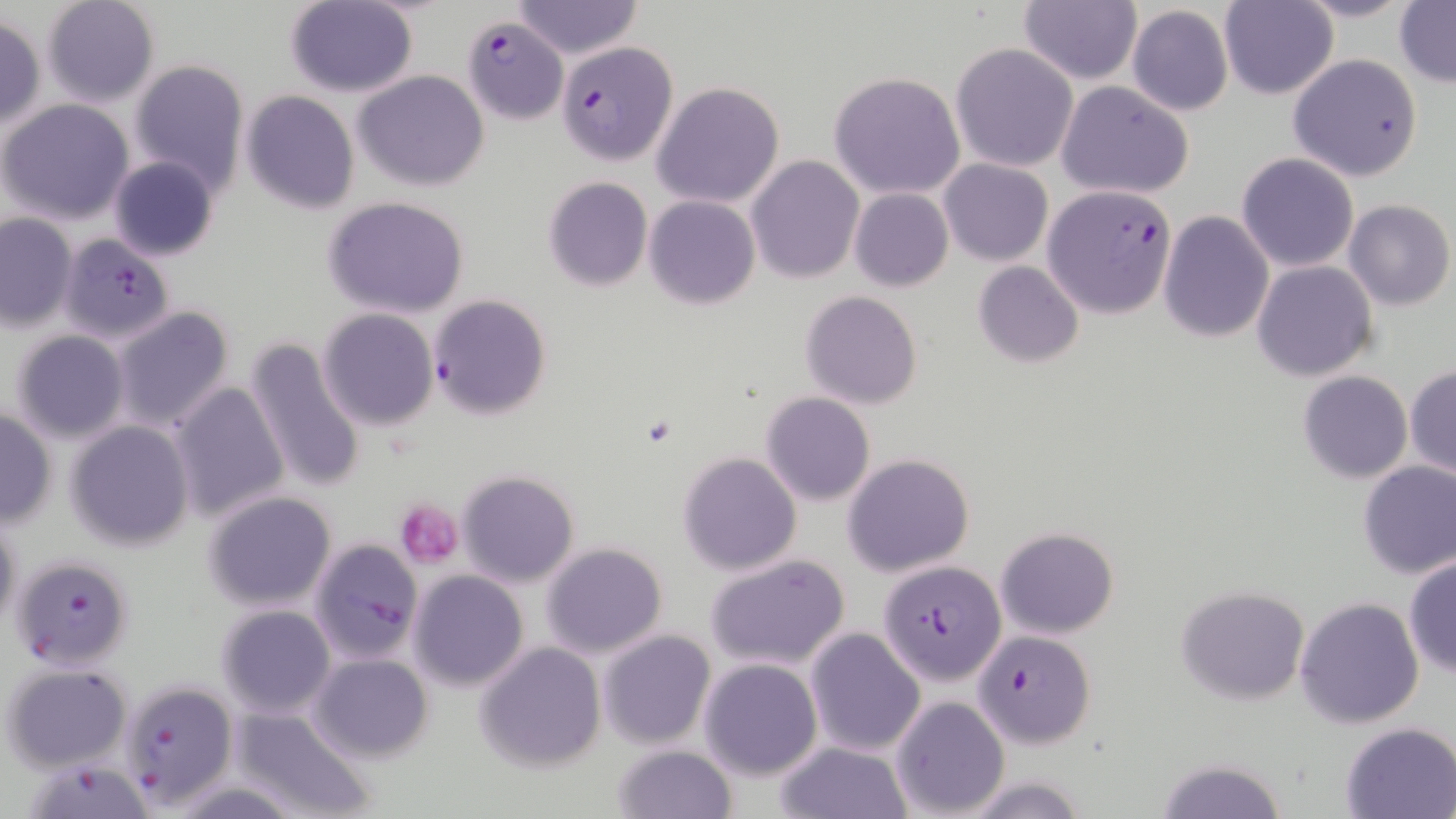
{
  "slide_level_diagnosis": "Plasmodium falciparum",
  "field_of_view": "one of a larger specimen",
  "plasmodium_falciparum_infected_red_blood_cell_locations": "approximate bounding boxes as (x1,y1)-(x2,y2) corner pairs in pixels: (462,16)-(569,124), (556,39)-(679,166), (1045,184)-(1178,320), (64,235)-(185,349), (428,294)-(551,421), (308,537)-(424,665), (8,555)-(135,672), (877,559)-(1005,685), (975,630)-(1098,746), (115,679)-(238,808), (23,758)-(156,819)",
  "image_size": "1456×819 pixels",
  "stain": "May-Grünwald-Giemsa",
  "magnification": "1000x",
  "uninfected_red_blood_cell_locations": "approximate bounding boxes as (x1,y1)-(x2,y2) corner pairs in pixels: (41,0)-(160,106), (283,0)-(419,97), (1020,0)-(1142,84), (1219,0)-(1337,100), (1294,0)-(1418,23), (510,1)-(644,59), (1395,2)-(1456,84), (1126,5)-(1234,116), (0,14)-(46,131), (951,44)-(1078,171), (1288,54)-(1423,181), (129,59)-(250,196), (354,69)-(490,191), (829,71)-(965,199), (652,81)-(785,209), (1055,82)-(1195,199), (241,91)-(359,213), (2,100)-(134,225), (1236,153)-(1360,273), (747,155)-(864,284), (108,156)-(220,262), (938,158)-(1053,265), (542,177)-(652,291), (848,187)-(954,292), (644,194)-(761,308), (322,197)-(471,318), (1343,199)-(1454,310), (1158,211)-(1274,343), (0,212)-(78,332), (1251,260)-(1378,382), (972,261)-(1084,368), (800,292)-(923,409), (110,305)-(236,433), (318,309)-(437,429), (9,329)-(131,443), (245,337)-(367,492), (1406,364)-(1456,478), (1297,371)-(1413,483), (167,381)-(290,523), (761,391)-(875,506), (1,407)-(55,527), (66,420)-(194,551), (678,452)-(800,574), (842,454)-(973,576), (1357,461)-(1456,579), (457,468)-(579,587), (203,491)-(337,611), (0,511)-(21,637), (996,528)-(1119,639), (541,543)-(667,659), (706,555)-(850,671), (1403,555)-(1456,678), (409,571)-(528,691), (1176,585)-(1309,705), (1295,596)-(1425,728), (216,605)-(336,719), (805,628)-(926,756), (599,629)-(716,749), (474,642)-(606,772), (310,653)-(432,762), (699,659)-(822,779), (3,662)-(133,771), (891,696)-(1010,817), (228,706)-(376,819), (1339,721)-(1456,819), (775,740)-(914,819), (612,744)-(737,819), (1154,757)-(1290,819), (160,780)-(309,817)",
  "preparation": "thin blood smear",
  "platelet_locations": "approximate bounding boxes as (x1,y1)-(x2,y2) corner pairs in pixels: (393,499)-(464,570)",
  "modality": "optical microscopy"
}